Classify this cell by malaria status.
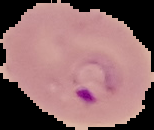

It is parasitized.

Image is 154×130 pixels. The area outside the segmented cell region is set to black. From a thin blood smear.